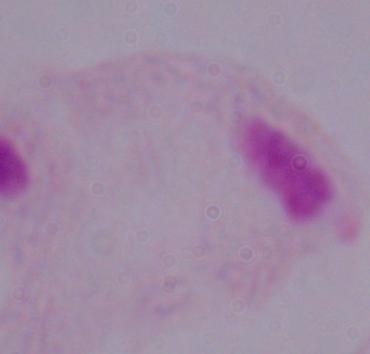
{
  "magnification": "1000x",
  "modality": "photomicrograph",
  "identification": "trichomonad"
}